Point out each Plasmodium parasite.
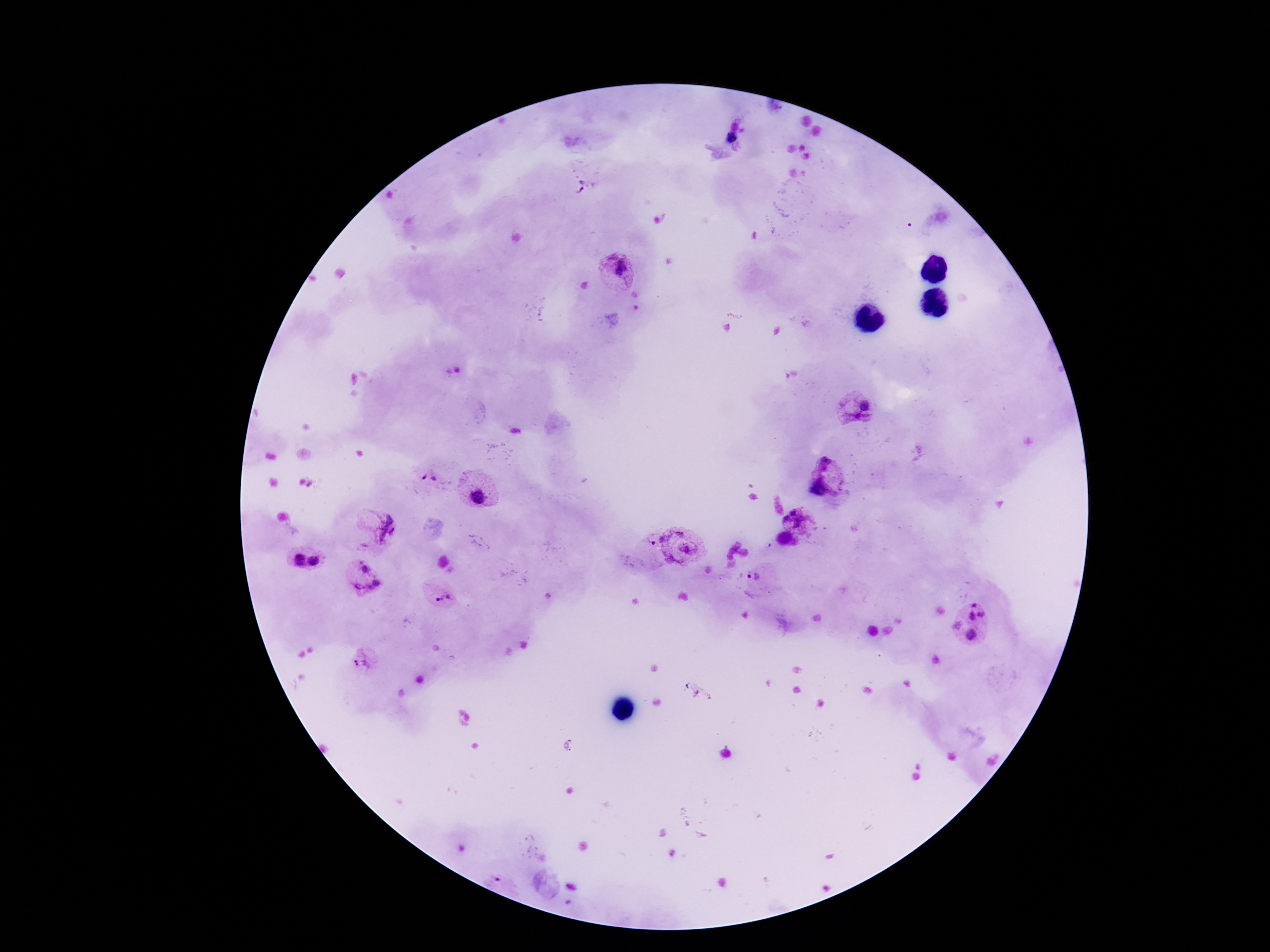

Approximate centers as {x, y} in pixels.
Plasmodium parasites: {733, 139}, {585, 186}, {617, 271}, {454, 373}, {856, 410}, {428, 478}, {824, 478}, {479, 498}, {800, 520}, {384, 531}, {647, 544}, {683, 545}, {298, 560}, {315, 563}, {757, 578}, {441, 597}, {978, 611}, {972, 635}, {363, 660}, {497, 882}.

stain = Giemsa
magnification = 100x
preparation = thick blood smear
image size = 1270×952 pixels
patient malaria status = positive
capture = smartphone camera through the microscope eyepiece
field of view = one from this slide